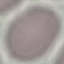
result: negative for malaria parasites
image_type: automatically extracted cell patch, resized to 64 × 64 pixels
capture: smartphone camera at the microscope eyepiece
stain: Giemsa
preparation: thin blood smear